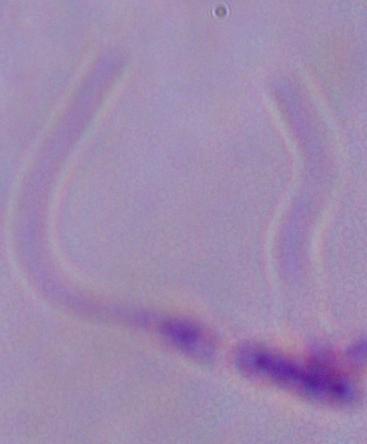
Photomicrograph. A Leishmania parasite is seen. 1000x magnification.